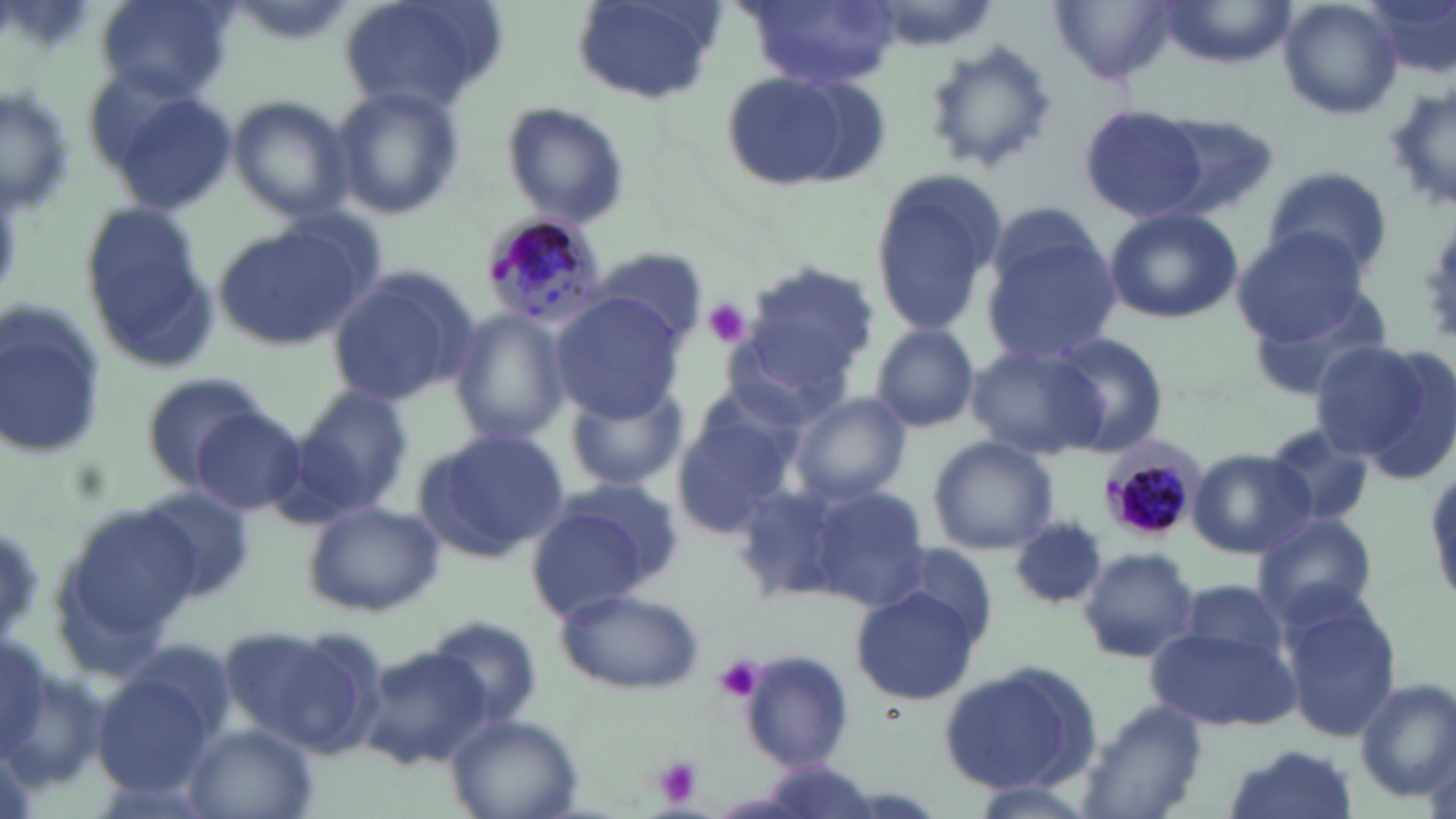 Approximate bounding boxes as [x1, y1, x2, y2] in pixels. Plasmodium malariae-infected red blood cell locations: [479, 213, 608, 331], [1098, 439, 1204, 546]. Uninfected red blood cell locations: [94, 0, 233, 100], [334, 0, 507, 117], [742, 0, 897, 89], [1160, 0, 1294, 66], [1276, 0, 1403, 120], [1366, 0, 1456, 85], [1052, 1, 1180, 84], [571, 2, 725, 108], [921, 39, 1059, 174], [720, 70, 881, 192], [1386, 80, 1456, 219], [96, 81, 237, 216], [1, 82, 75, 217], [330, 84, 465, 220], [228, 94, 355, 221], [1077, 102, 1212, 225], [503, 104, 629, 228], [1148, 113, 1282, 220], [1263, 164, 1392, 277], [869, 170, 1007, 339], [77, 200, 215, 369], [1104, 207, 1243, 324], [980, 214, 1122, 366], [207, 219, 371, 353], [1231, 228, 1369, 344], [590, 245, 711, 348], [743, 262, 880, 390], [326, 264, 479, 409], [1245, 284, 1395, 402], [549, 294, 687, 419], [0, 303, 107, 463], [449, 309, 572, 446], [871, 324, 980, 433], [1045, 332, 1171, 456], [1305, 338, 1444, 464], [966, 341, 1107, 461], [137, 370, 274, 484], [560, 380, 689, 492], [296, 385, 413, 510], [789, 392, 912, 505], [671, 405, 804, 540], [191, 408, 309, 515], [1262, 425, 1379, 529], [412, 430, 569, 562], [926, 436, 1059, 555], [1188, 449, 1316, 558], [803, 484, 929, 611], [137, 485, 259, 602], [527, 485, 681, 614], [301, 500, 447, 617], [59, 504, 209, 656], [1250, 512, 1380, 629], [1010, 519, 1107, 613], [1078, 547, 1201, 662], [1176, 577, 1294, 670], [850, 585, 984, 706], [555, 587, 704, 693], [1281, 597, 1402, 745], [423, 617, 546, 726], [232, 621, 386, 759], [1146, 624, 1301, 734], [361, 647, 492, 770], [736, 650, 854, 771], [938, 659, 1102, 796], [92, 669, 219, 798], [1353, 678, 1455, 803], [1076, 700, 1209, 819], [445, 712, 583, 819], [184, 724, 319, 818], [1220, 744, 1357, 819], [966, 780, 1100, 819]. Platelet locations: [704, 300, 752, 349], [713, 656, 764, 704], [650, 756, 703, 806]. Slide-level diagnosis: Plasmodium malariae. Thin blood smear. Light microscopy. Image is 1456×819 pixels. May-Grünwald-Giemsa stain. Single field of view. Captured at 1000x magnification.